Locate every malaria parasite and every leukocyte.
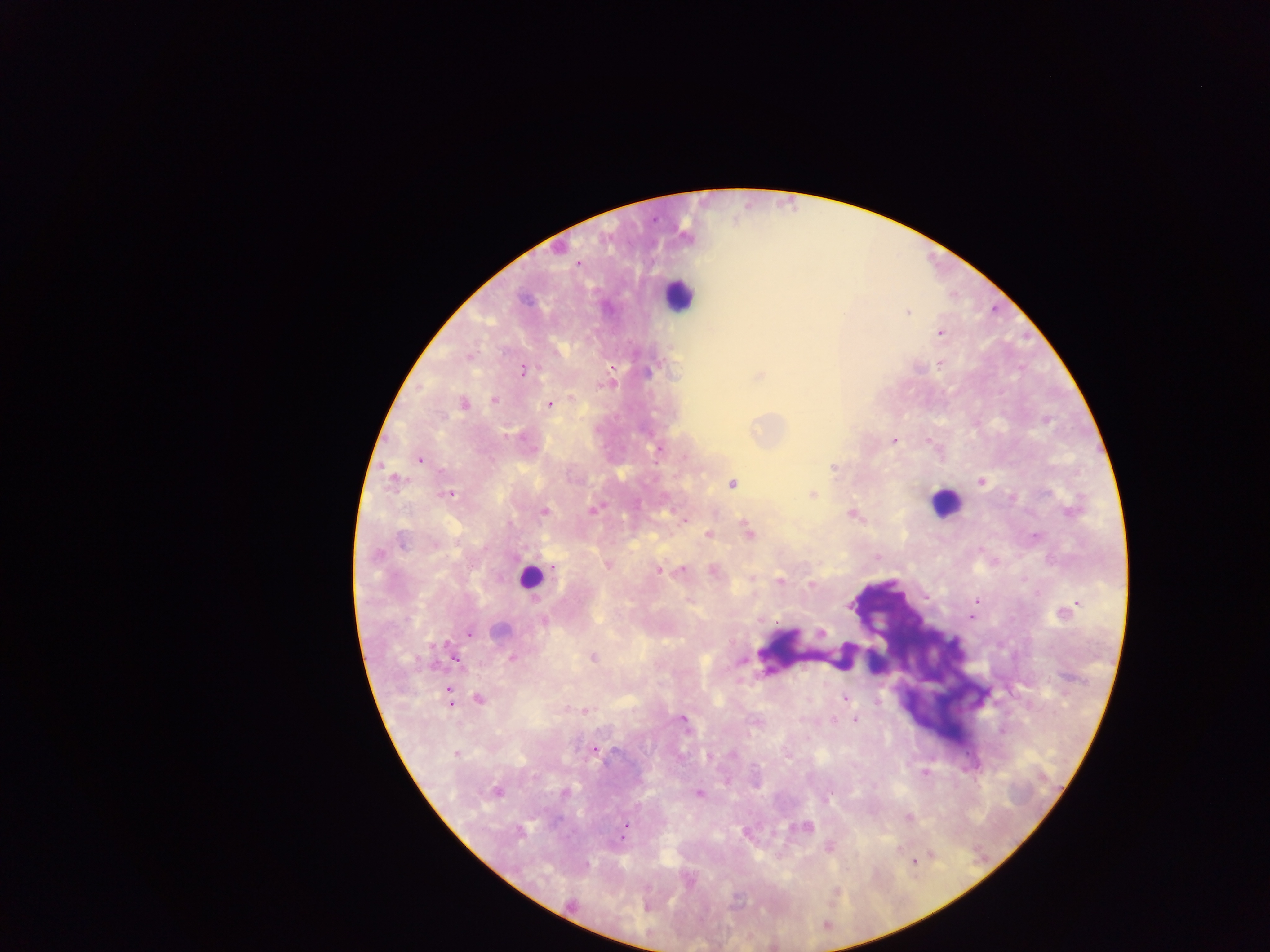
Approximate centers as {x, y} in pixels.
Malaria parasites: {576, 264}, {907, 312}, {941, 333}, {468, 356}, {940, 363}, {611, 369}, {522, 371}, {757, 376}, {494, 399}, {463, 404}, {549, 404}, {893, 440}, {659, 448}, {419, 459}, {833, 468}, {395, 479}, {981, 480}, {732, 483}, {447, 494}, {812, 494}, {593, 509}, {543, 511}, {852, 514}, {684, 519}, {748, 531}, {708, 534}, {877, 557}, {607, 565}, {552, 566}, {657, 570}, {681, 570}, {712, 570}, {751, 577}, {779, 582}, {811, 584}, {925, 597}, {977, 601}, {1074, 605}, {1067, 611}, {972, 616}, {544, 622}, {821, 632}, {469, 633}, {512, 657}, {592, 657}, {455, 658}, {844, 697}, {478, 698}, {449, 699}, {584, 710}, {682, 719}, {833, 719}, {855, 719}, {594, 749}, {456, 753}, {708, 756}, {924, 772}, {564, 791}, {495, 792}, {698, 792}, {908, 817}, {625, 827}, {805, 827}, {828, 846}, {915, 859}, {835, 891}.
Leukocytes: {677, 295}, {945, 503}, {529, 576}.

Collected in Ghana. Single field of view. Thick blood smear. Mobile-phone photograph taken through the microscope. Image is 1270×952 pixels.